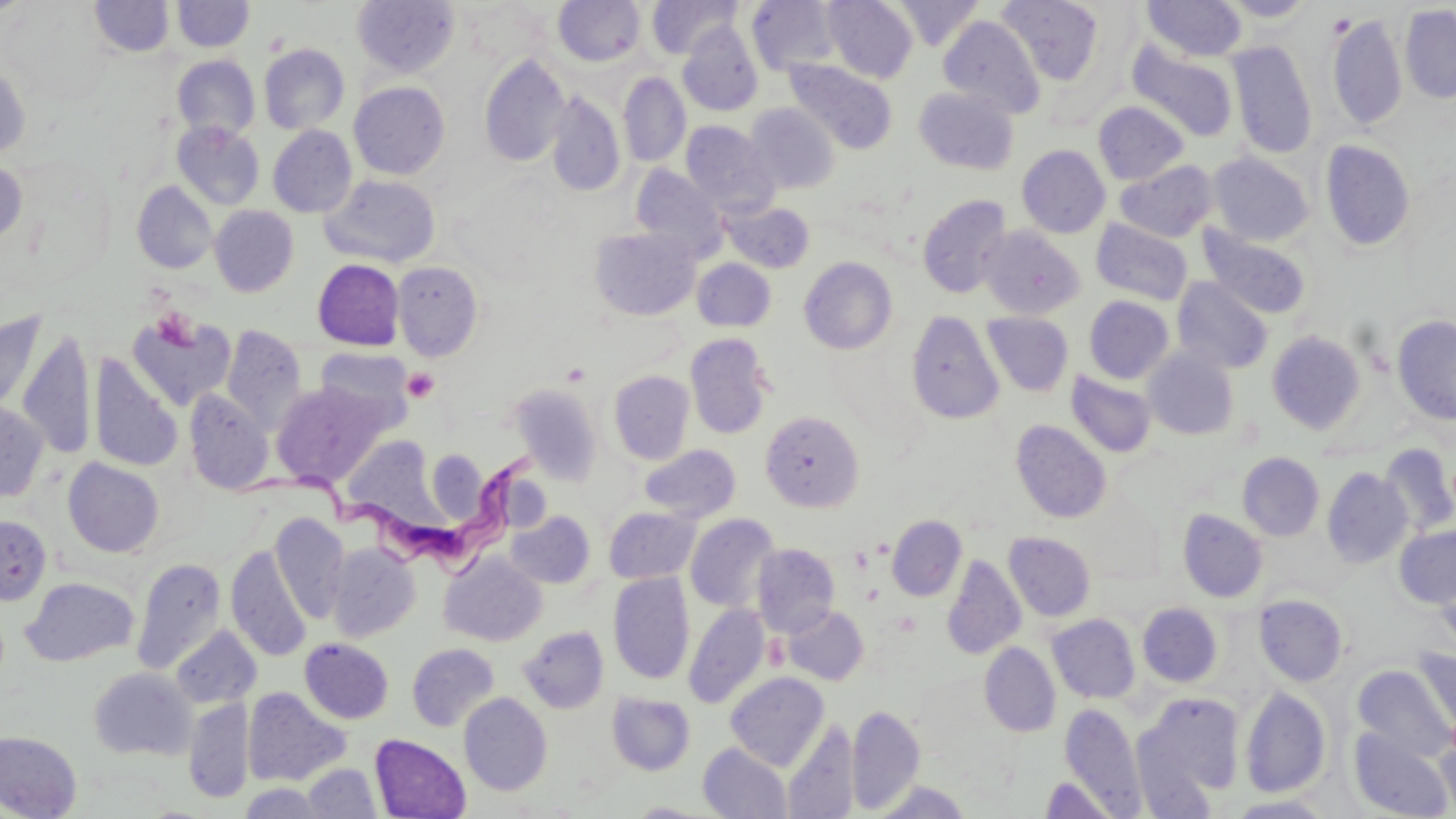
Summary:
  - Coordinate format: approximate bounding boxes as (x1, y1, x2, y2) in pixels
  - Uninfected red blood cell locations: (89, 0, 175, 57), (553, 0, 645, 66), (646, 0, 741, 59), (823, 0, 918, 83), (892, 0, 983, 51), (998, 0, 1104, 86), (1218, 0, 1318, 22), (172, 1, 254, 52), (351, 1, 460, 79), (747, 1, 842, 76), (1142, 1, 1247, 61), (1, 2, 114, 105), (1400, 4, 1456, 103), (1327, 13, 1408, 130), (939, 16, 1045, 119), (678, 21, 763, 116), (1127, 40, 1239, 142), (1227, 41, 1318, 158), (259, 43, 350, 135), (479, 53, 570, 167), (172, 55, 260, 140), (0, 58, 31, 161), (785, 60, 898, 154), (618, 72, 690, 168), (349, 82, 450, 180), (914, 87, 1019, 175), (545, 92, 625, 197), (1093, 101, 1189, 185), (745, 103, 839, 194), (172, 120, 265, 210), (681, 122, 780, 217), (268, 125, 357, 217), (1320, 139, 1415, 252), (1017, 144, 1111, 238), (1208, 151, 1314, 246), (0, 158, 27, 246), (1115, 160, 1218, 242), (631, 164, 728, 262), (320, 174, 441, 267), (131, 181, 218, 274), (917, 195, 1014, 298), (722, 200, 815, 273), (209, 205, 299, 297), (1091, 219, 1193, 306), (979, 226, 1085, 319), (1199, 226, 1311, 319), (590, 227, 700, 320), (799, 257, 897, 354), (312, 259, 404, 350), (692, 259, 776, 332), (392, 261, 484, 361), (1172, 277, 1273, 374), (1083, 295, 1174, 384), (906, 309, 1005, 425), (127, 310, 237, 411), (0, 311, 47, 413), (982, 312, 1073, 397), (1392, 315, 1456, 425), (220, 325, 306, 435), (17, 329, 97, 459), (1267, 331, 1365, 433), (684, 332, 774, 440), (314, 347, 415, 434), (1143, 348, 1239, 441), (89, 353, 184, 472), (1065, 369, 1157, 459), (608, 370, 695, 465), (271, 381, 389, 486), (509, 384, 602, 484), (183, 387, 275, 494), (0, 399, 49, 502), (760, 411, 865, 512), (1010, 419, 1111, 524), (343, 436, 441, 525), (640, 444, 741, 522), (1379, 444, 1456, 537), (423, 449, 492, 531), (1238, 453, 1325, 541), (63, 457, 164, 557), (1322, 468, 1412, 568), (604, 506, 699, 584), (1178, 509, 1268, 602), (506, 511, 595, 589), (269, 512, 350, 622), (685, 513, 780, 612), (0, 515, 52, 604), (887, 515, 966, 601), (1394, 524, 1456, 608), (1003, 532, 1095, 621), (326, 542, 421, 642), (752, 543, 840, 637), (226, 545, 311, 663), (439, 551, 547, 646), (942, 554, 1027, 659), (131, 558, 227, 675), (1435, 563, 1456, 655), (608, 572, 695, 685), (20, 576, 139, 667), (1254, 594, 1348, 686), (683, 603, 771, 709), (1137, 603, 1222, 687), (782, 605, 869, 685), (1047, 614, 1140, 704), (170, 626, 262, 709), (518, 626, 609, 714), (299, 638, 394, 724), (980, 642, 1061, 736), (406, 643, 499, 732), (1412, 646, 1456, 737), (1002, 658, 1084, 753), (1353, 665, 1455, 762), (89, 667, 197, 761), (725, 672, 829, 771), (1240, 686, 1331, 798), (242, 687, 349, 786), (607, 692, 695, 776), (1137, 692, 1244, 801), (459, 693, 552, 796), (183, 698, 255, 804), (1059, 703, 1147, 816), (846, 704, 925, 813), (783, 719, 860, 819), (1348, 728, 1454, 818), (0, 731, 82, 818), (370, 734, 470, 818), (1434, 734, 1456, 816), (698, 743, 792, 819), (303, 763, 381, 818), (1039, 776, 1119, 819), (869, 780, 974, 818), (239, 782, 329, 819), (1225, 795, 1338, 818), (627, 802, 717, 817)
  - Trypanosoma brucei locations: (247, 440, 535, 569)
  - Platelet locations: (153, 309, 196, 349), (402, 368, 440, 402)
  - Slide-level diagnosis: Trypanosoma brucei
  - Stain: May-Grünwald-Giemsa
  - Magnification: 1000x
  - Image size: 1456×819 pixels
  - Modality: optical microscopy
  - Field of view: single
  - Preparation: thin blood film